Assess this cell for malaria.
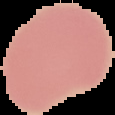

Uninfected.

From a thin blood smear. Image is 115×115 pixels. Segmented cell region on a black background.